Locate every blood parasite and identify its species.
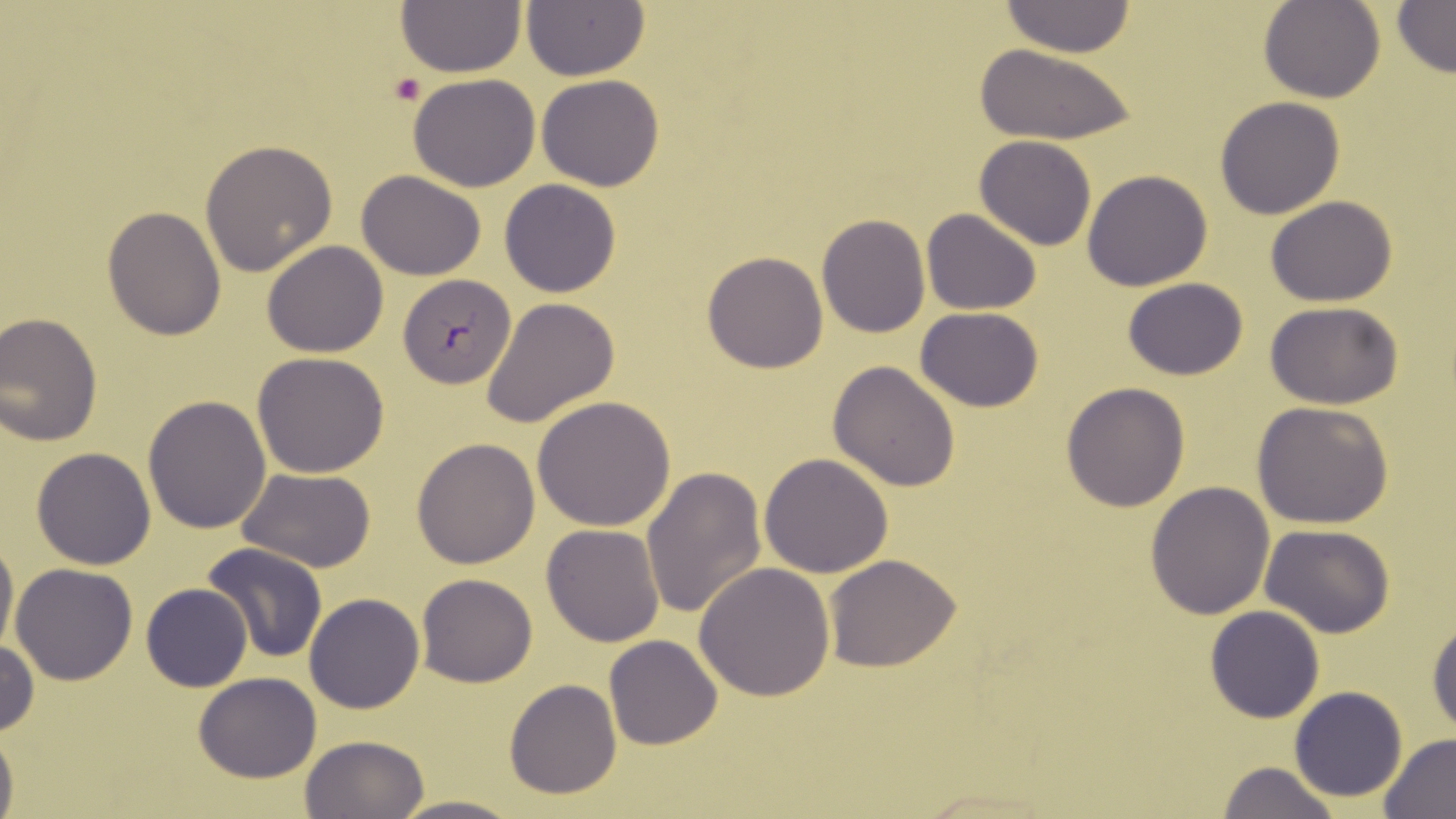

Approximate bounding boxes as [x1, y1, x2, y2] in pixels.
Plasmodium falciparum-infected red blood cells: [399, 274, 515, 387].
No Plasmodium ovale, Plasmodium malariae, Plasmodium vivax, Babesia divergens, or Trypanosoma brucei observed.

Summary:
  - Uninfected red blood cell locations: [394, 1, 528, 78], [999, 1, 1136, 57], [1260, 1, 1383, 103], [522, 2, 650, 81], [1393, 2, 1455, 75], [972, 43, 1138, 145], [407, 73, 541, 192], [536, 74, 665, 191], [1214, 97, 1345, 220], [975, 136, 1097, 250], [200, 139, 337, 277], [1081, 169, 1212, 291], [357, 170, 485, 279], [501, 179, 620, 296], [1265, 195, 1396, 306], [102, 206, 228, 340], [921, 208, 1043, 314], [816, 213, 930, 338], [261, 240, 388, 357], [702, 251, 829, 373], [1123, 278, 1249, 380], [481, 297, 622, 429], [1264, 301, 1403, 409], [915, 307, 1043, 411], [0, 311, 103, 447], [253, 351, 390, 478], [828, 361, 962, 491], [1061, 381, 1190, 511], [142, 395, 272, 534], [532, 396, 677, 531], [1251, 401, 1393, 529], [411, 438, 540, 568], [32, 447, 157, 569], [759, 452, 893, 578], [237, 467, 376, 571], [641, 467, 765, 620], [1145, 480, 1275, 620], [541, 523, 667, 647], [1260, 524, 1393, 638], [0, 531, 18, 659], [203, 543, 328, 663], [824, 555, 962, 673], [694, 562, 838, 703], [9, 563, 138, 686], [416, 573, 538, 688], [141, 582, 252, 692], [304, 592, 425, 714], [1204, 604, 1326, 722], [1426, 612, 1456, 735], [604, 634, 723, 750], [0, 637, 38, 739], [193, 673, 322, 783], [504, 679, 622, 800], [1288, 686, 1408, 802], [0, 723, 18, 819], [1380, 733, 1456, 819], [299, 734, 429, 819], [1215, 761, 1342, 819], [392, 792, 520, 819]
  - Platelet locations: [390, 74, 426, 105]
  - Slide-level diagnosis: Plasmodium falciparum
  - Field of view: one of a larger specimen
  - Image size: 1456×819 pixels
  - Modality: optical microscopy
  - Preparation: thin blood smear
  - Magnification: 1000x
  - Stain: May-Grünwald-Giemsa